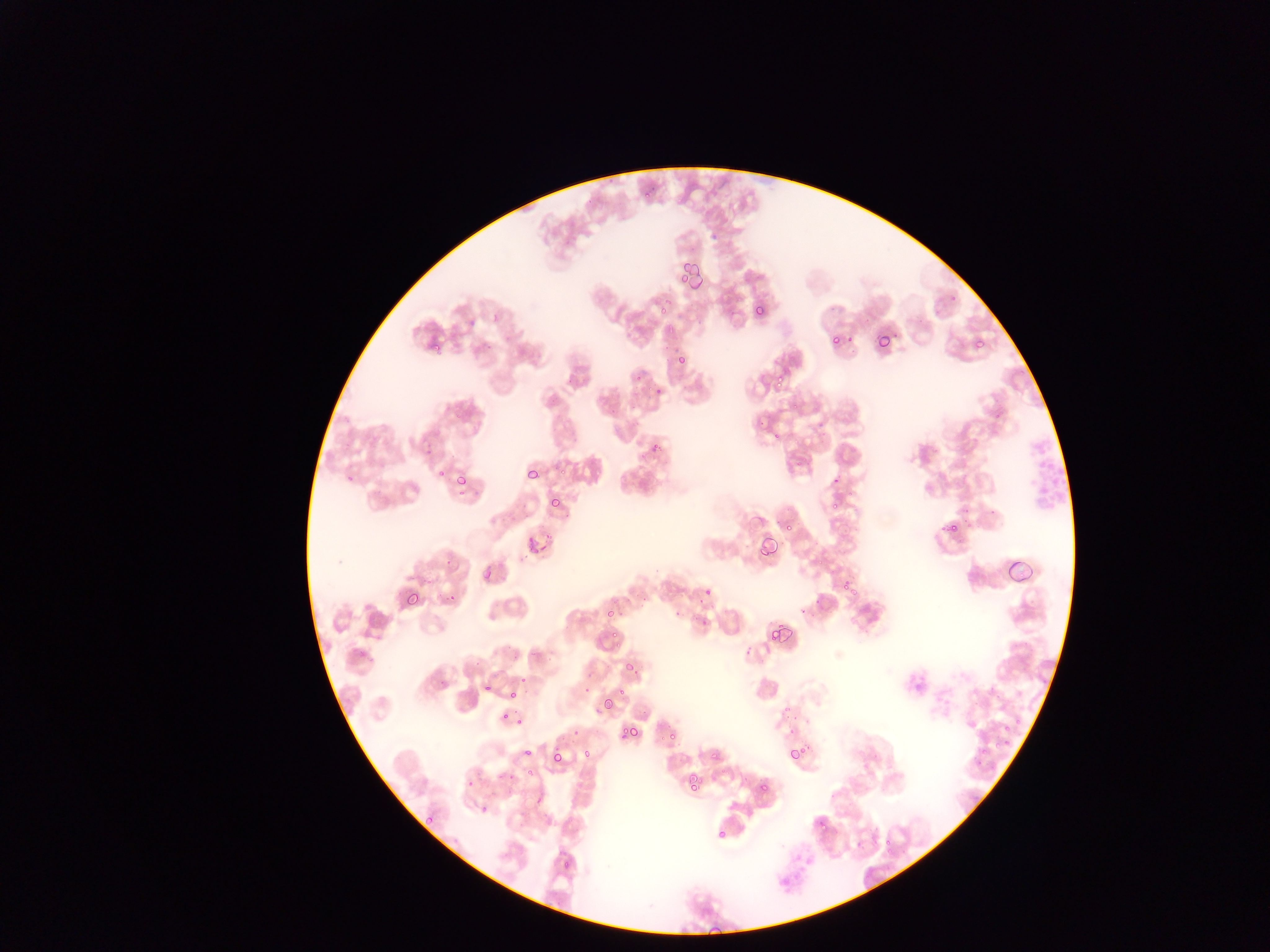

Approximate bounding boxes as {left, top, right, bottom} in pixels.
Summary:
  - Malaria parasite locations: {674, 257, 692, 286}, {688, 263, 710, 297}, {752, 303, 768, 320}, {656, 304, 675, 316}, {828, 333, 842, 349}, {875, 334, 894, 354}, {971, 337, 987, 352}, {429, 344, 445, 353}, {674, 350, 689, 367}, {767, 372, 791, 392}, {787, 397, 803, 414}, {769, 428, 783, 444}, {649, 441, 666, 453}, {432, 465, 445, 481}, {527, 467, 540, 480}, {448, 470, 473, 485}, {547, 495, 561, 510}, {827, 498, 845, 517}, {939, 519, 966, 535}, {784, 520, 797, 534}, {523, 534, 544, 556}, {759, 538, 778, 559}, {1006, 555, 1038, 587}, {482, 568, 497, 583}, {839, 576, 859, 597}, {700, 582, 715, 598}, {404, 589, 423, 608}, {444, 592, 459, 609}, {603, 602, 619, 622}, {767, 622, 789, 645}, {607, 625, 624, 641}, {625, 661, 639, 676}, {615, 684, 628, 699}, {505, 693, 521, 704}, {600, 704, 615, 715}, {1010, 713, 1026, 733}, {500, 714, 509, 725}, {509, 714, 526, 734}, {663, 723, 680, 743}, {623, 725, 641, 743}, {997, 736, 1014, 754}, {521, 739, 537, 755}, {581, 744, 595, 760}, {787, 745, 803, 763}, {550, 747, 569, 767}, {706, 748, 725, 765}, {500, 764, 520, 790}, {525, 769, 536, 777}, {681, 772, 702, 798}, {466, 780, 476, 789}, {755, 780, 769, 794}, {479, 805, 490, 817}, {421, 809, 437, 825}, {814, 816, 829, 833}, {716, 829, 729, 842}, {881, 836, 898, 855}, {560, 858, 576, 871}, {705, 926, 722, 936}
  - Leukocyte locations: {1024, 424, 1072, 515}
  - Country: Ghana
  - Field of view: single
  - Preparation: thin blood smear
  - Image size: 1270×952 pixels
  - Capture: mobile-phone photograph through a microscope